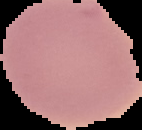
image size = 142×130 pixels
preparation = thin blood film
malaria status = uninfected
image type = cell region segmented out of the field of view; surrounding area masked to black